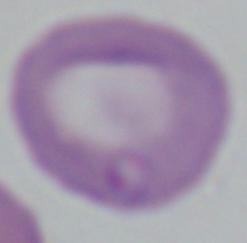

Summary:
  - Modality: photomicrograph
  - Magnification: 1000x
  - Identification: Babesia